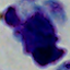

identification = white blood cell
magnification = 1000x
modality = micrograph